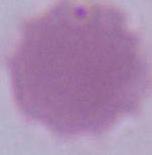

Summary:
  - Magnification: 1000x
  - Identification: erythrocyte
  - Modality: photomicrograph